Assess this cell for malaria.
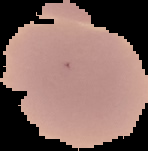

It is uninfected.

preparation = thin blood smear
image type = cell region segmented out of the field of view; surrounding area masked to black
image size = 148×151 pixels